Give the extent of all Plasmodium falciparum-infected red blood cells.
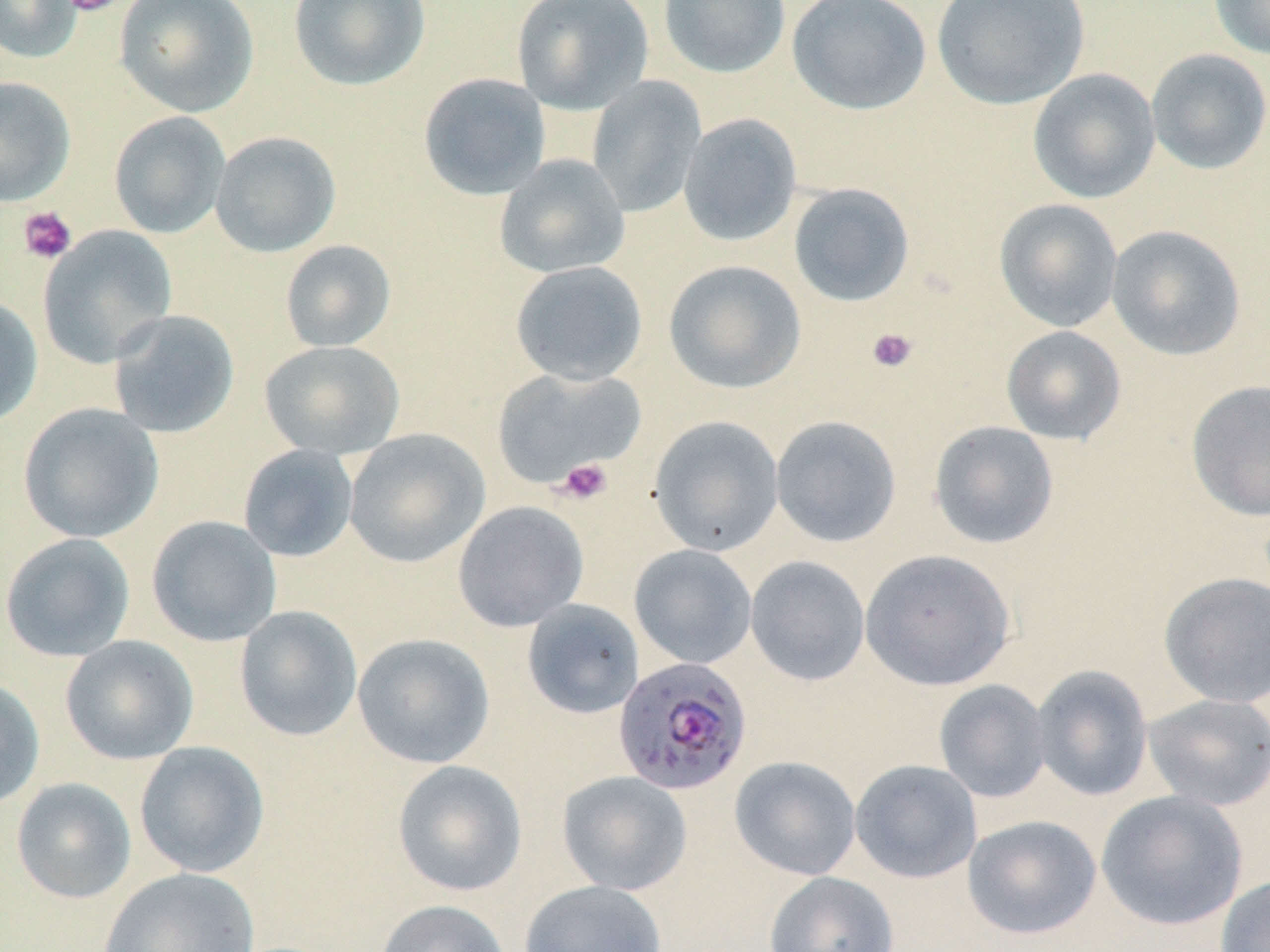
Approximate bounding boxes as named x1/y1/x2/y2 corners in pixels.
Plasmodium falciparum-infected red blood cells: (x1=613, y1=657, x2=752, y2=796).

Uninfected red blood cell locations: (x1=0, y1=0, x2=82, y2=63), (x1=114, y1=0, x2=259, y2=118), (x1=287, y1=0, x2=430, y2=91), (x1=511, y1=0, x2=654, y2=115), (x1=658, y1=0, x2=791, y2=78), (x1=787, y1=0, x2=932, y2=115), (x1=931, y1=0, x2=1090, y2=109), (x1=1208, y1=0, x2=1270, y2=60), (x1=1146, y1=48, x2=1270, y2=174), (x1=1027, y1=68, x2=1161, y2=204), (x1=418, y1=72, x2=551, y2=200), (x1=587, y1=75, x2=707, y2=218), (x1=0, y1=76, x2=76, y2=206), (x1=108, y1=111, x2=231, y2=239), (x1=678, y1=113, x2=802, y2=247), (x1=210, y1=131, x2=341, y2=257), (x1=494, y1=154, x2=630, y2=278), (x1=788, y1=182, x2=915, y2=307), (x1=993, y1=198, x2=1123, y2=332), (x1=1106, y1=224, x2=1246, y2=361), (x1=37, y1=225, x2=177, y2=368), (x1=279, y1=240, x2=397, y2=352), (x1=509, y1=260, x2=648, y2=386), (x1=663, y1=260, x2=807, y2=394), (x1=0, y1=295, x2=43, y2=429), (x1=108, y1=309, x2=240, y2=438), (x1=1001, y1=325, x2=1126, y2=445), (x1=259, y1=340, x2=405, y2=459), (x1=491, y1=366, x2=645, y2=489), (x1=1185, y1=379, x2=1270, y2=521), (x1=18, y1=402, x2=164, y2=543), (x1=770, y1=415, x2=902, y2=547), (x1=648, y1=416, x2=785, y2=557), (x1=929, y1=420, x2=1059, y2=550), (x1=344, y1=428, x2=490, y2=568), (x1=238, y1=444, x2=358, y2=562), (x1=452, y1=500, x2=589, y2=632), (x1=146, y1=515, x2=282, y2=646), (x1=0, y1=532, x2=136, y2=662), (x1=629, y1=544, x2=757, y2=669), (x1=860, y1=549, x2=1016, y2=691), (x1=746, y1=555, x2=870, y2=686), (x1=1158, y1=571, x2=1270, y2=708), (x1=522, y1=600, x2=644, y2=719), (x1=235, y1=605, x2=363, y2=741), (x1=352, y1=633, x2=494, y2=769), (x1=60, y1=635, x2=198, y2=765), (x1=1030, y1=665, x2=1153, y2=801), (x1=0, y1=676, x2=45, y2=811), (x1=934, y1=679, x2=1051, y2=803), (x1=1142, y1=693, x2=1270, y2=811), (x1=134, y1=741, x2=269, y2=877), (x1=729, y1=755, x2=861, y2=880), (x1=392, y1=759, x2=528, y2=897), (x1=850, y1=759, x2=982, y2=883), (x1=557, y1=771, x2=692, y2=895), (x1=11, y1=777, x2=136, y2=904), (x1=1095, y1=790, x2=1249, y2=931), (x1=962, y1=814, x2=1102, y2=939), (x1=100, y1=867, x2=259, y2=952), (x1=764, y1=871, x2=899, y2=952), (x1=1215, y1=875, x2=1270, y2=952), (x1=519, y1=880, x2=667, y2=952), (x1=375, y1=898, x2=511, y2=952). Platelet locations: (x1=60, y1=0, x2=123, y2=16), (x1=18, y1=206, x2=77, y2=264), (x1=866, y1=327, x2=918, y2=373), (x1=556, y1=458, x2=613, y2=505). Slide-level diagnosis: Plasmodium falciparum. Light microscopy. Image is 1270×952 pixels. Thin blood film. May-Grünwald-Giemsa-stained preparation. Captured at 1000x magnification. One field of a larger specimen.